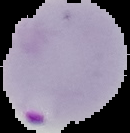

image_size: 130×133 pixels
preparation: thin blood film
image_type: segmented cell region on a black background
malaria_status: parasitized